Locate and identify every blood parasite.
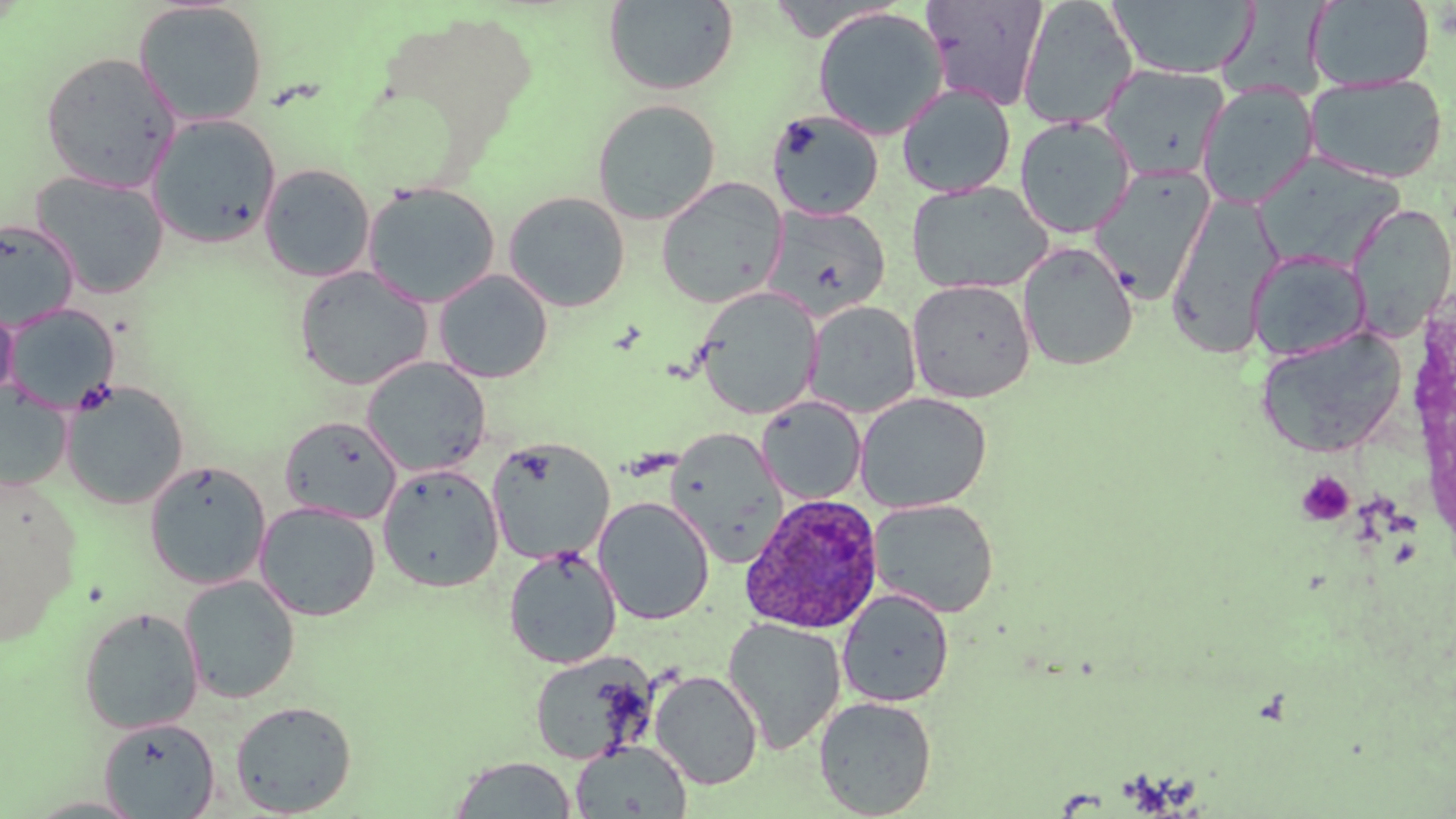

Approximate bounding boxes as (x1, y1, x2, y2) in pixels.
Plasmodium ovale-infected red blood cells: (740, 494, 885, 634).
No Plasmodium falciparum, Plasmodium malariae, Plasmodium vivax, Babesia divergens, or Trypanosoma brucei observed.

Summary:
  - Platelet locations: (1296, 471, 1356, 526)
  - Uninfected red blood cell locations: (765, 0, 902, 41), (922, 0, 1049, 111), (1106, 0, 1258, 80), (1306, 0, 1435, 91), (133, 1, 268, 127), (603, 1, 739, 95), (1017, 1, 1139, 130), (813, 7, 948, 140), (40, 51, 181, 193), (1099, 64, 1231, 181), (1305, 74, 1448, 184), (1196, 82, 1319, 209), (896, 83, 1017, 198), (592, 99, 721, 225), (766, 109, 884, 221), (147, 113, 282, 249), (1014, 116, 1137, 239), (1254, 153, 1409, 269), (259, 163, 375, 283), (1089, 164, 1216, 303), (30, 170, 170, 299), (656, 176, 788, 308), (905, 180, 1054, 295), (362, 181, 501, 308), (503, 191, 631, 312), (1165, 193, 1283, 359), (1348, 203, 1455, 342), (761, 204, 891, 322), (0, 219, 79, 329), (1018, 242, 1139, 372), (1248, 249, 1371, 362), (293, 265, 433, 390), (433, 269, 553, 384), (906, 278, 1036, 403), (694, 286, 822, 420), (0, 298, 18, 404), (804, 300, 921, 418), (3, 304, 121, 414), (1255, 327, 1408, 458), (361, 356, 491, 477), (61, 381, 190, 509), (0, 383, 72, 489), (854, 392, 992, 513), (756, 396, 866, 505), (279, 415, 402, 524), (666, 427, 788, 564), (486, 437, 615, 565), (144, 460, 271, 590), (378, 464, 504, 592), (1, 479, 80, 647), (593, 496, 715, 625), (869, 498, 1000, 618), (254, 500, 382, 621), (503, 546, 621, 669), (178, 574, 301, 704), (836, 588, 954, 708), (77, 606, 204, 734), (722, 618, 846, 754), (527, 650, 656, 765), (649, 670, 763, 790), (813, 696, 937, 818), (230, 700, 358, 816), (99, 717, 221, 818), (569, 741, 691, 818), (450, 755, 578, 818), (21, 795, 150, 817)
  - Slide-level diagnosis: Plasmodium ovale
  - Stain: May-Grünwald-Giemsa
  - Modality: light microscopy
  - Magnification: 1000x
  - Preparation: thin blood film
  - Field of view: single
  - Image size: 1456×819 pixels